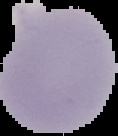 Result: no Plasmodium parasites seen. From a thin blood smear. Image is 118×136 pixels. Cell region segmented out of the field of view; the surrounding area is masked to black.